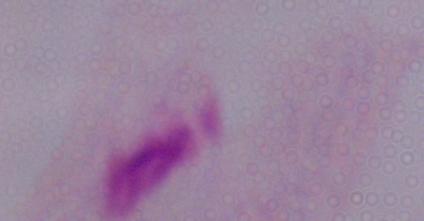
modality = photomicrograph
identification = trichomonad
magnification = 1000x